Comment on the morphology of the erythrocytes.
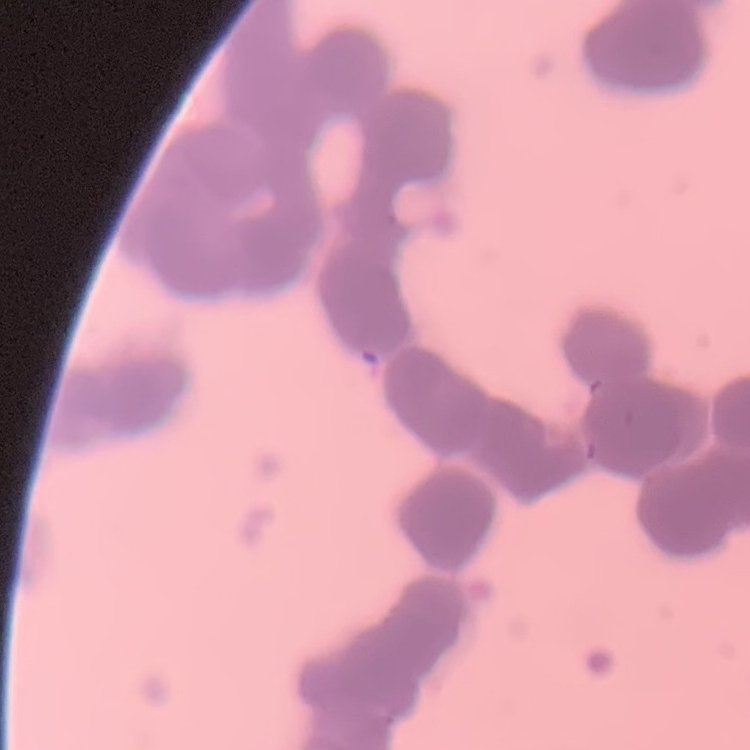

Rouleaux formation.

Summary:
  - Preparation: thin blood smear
  - Image type: one tile cut from a larger photomicrograph
  - Stain: Field's or Giemsa